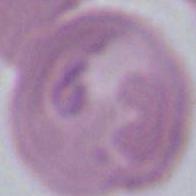
Summary:
  - Identification: red blood cell
  - Modality: photomicrograph
  - Magnification: 1000x